State which parasite is depicted.
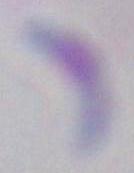
This is Toxoplasma gondii.

Captured at 1000x magnification. Photomicrograph.